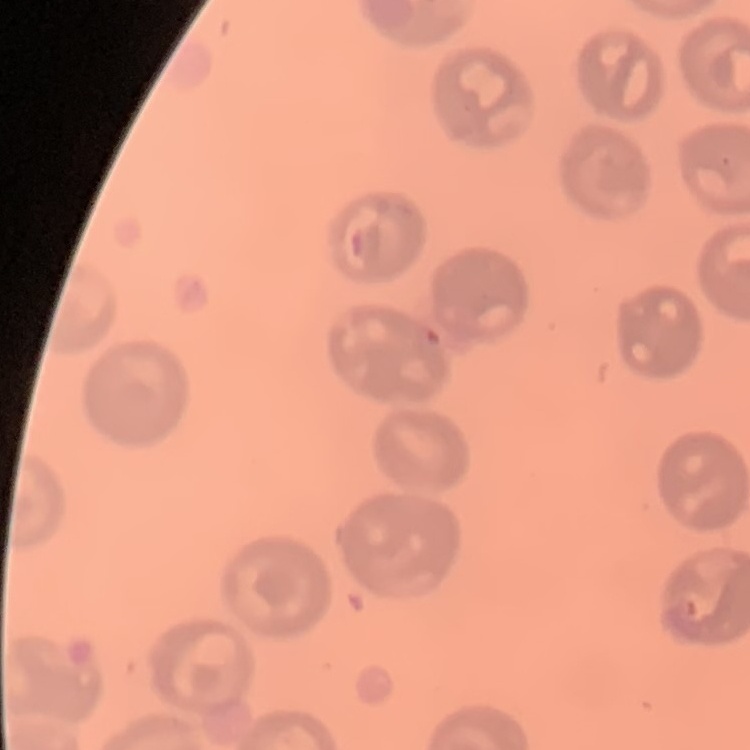 The erythrocytes exhibit no rouleaux formation. Field's or Giemsa stain. Thin blood film. One tile cut from a larger photomicrograph.